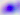

magnification = 400x
identification = Toxoplasma gondii
modality = photomicrograph